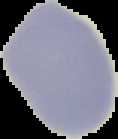
preparation: thin blood film
result: no malaria parasites seen
image_size: 118×139 pixels
image_type: segmented cell region on a black background